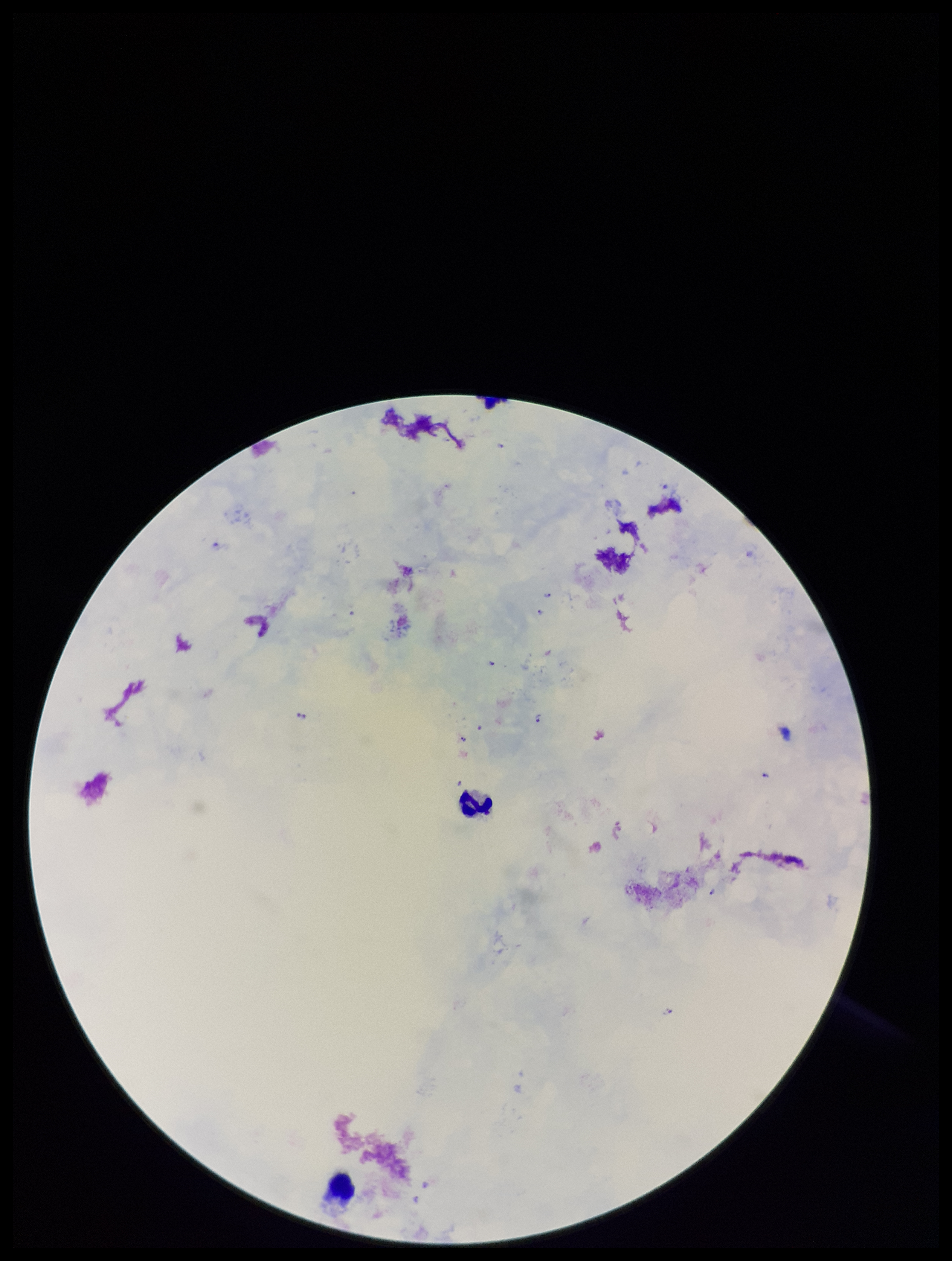
image size = 952×1261 pixels
Plasmodium parasites = identified
patient malaria status = positive
capture = smartphone photograph through the microscope eyepiece
preparation = thick
stain = Giemsa
parasite count = 10
species reported for this patient = Plasmodium falciparum
field of view = one from this slide
leukocyte count = 2